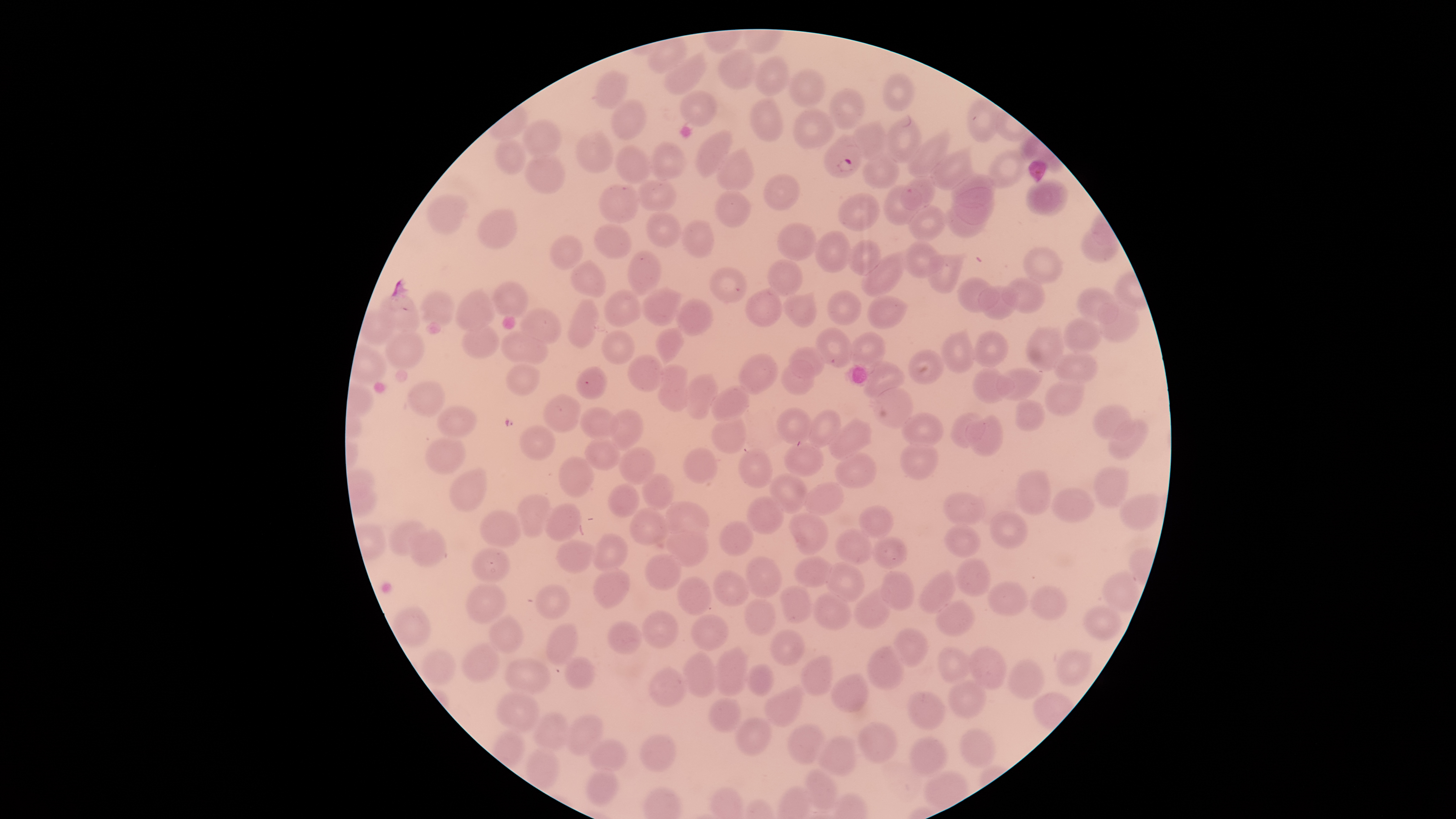
Approximate bounding boxes as [left, top, right, bottom] in pixels. Uninfected red blood cells: [649, 38, 686, 72], [719, 50, 757, 90], [666, 52, 708, 94], [754, 56, 791, 96], [595, 70, 629, 109], [788, 70, 825, 108], [883, 73, 914, 110], [830, 88, 864, 128], [679, 90, 717, 126], [967, 97, 999, 142], [750, 98, 785, 142], [611, 99, 646, 140], [793, 108, 833, 150], [885, 117, 923, 162], [524, 120, 563, 156], [852, 122, 887, 159], [577, 130, 613, 171], [696, 130, 733, 177], [908, 136, 947, 176], [494, 138, 526, 176], [651, 142, 686, 179], [617, 145, 650, 181], [987, 150, 1025, 187], [718, 151, 755, 189], [931, 152, 971, 189], [863, 153, 900, 189], [525, 155, 565, 194], [764, 173, 802, 210], [952, 175, 994, 208], [901, 178, 935, 209], [638, 179, 676, 211], [1026, 180, 1068, 214], [598, 184, 639, 224], [884, 186, 921, 226], [955, 188, 994, 225], [714, 189, 751, 227], [839, 193, 880, 231], [428, 194, 470, 237], [946, 205, 985, 237], [910, 206, 947, 240], [479, 209, 518, 247], [646, 212, 682, 247], [682, 220, 715, 257], [778, 223, 817, 260], [595, 224, 632, 258], [1081, 225, 1119, 263], [816, 231, 851, 271], [550, 235, 585, 269], [847, 241, 881, 276], [903, 241, 943, 279], [1023, 246, 1061, 284], [628, 251, 662, 293], [862, 253, 904, 295], [928, 254, 965, 293], [768, 259, 804, 296], [571, 260, 606, 296], [711, 268, 748, 303], [959, 278, 999, 313], [1003, 278, 1046, 313], [492, 282, 527, 317], [978, 286, 1020, 319], [1077, 286, 1119, 325], [642, 287, 682, 326], [455, 289, 495, 331], [746, 289, 784, 327], [420, 290, 456, 327], [604, 290, 642, 328], [828, 290, 862, 325], [783, 294, 816, 328], [865, 294, 907, 329], [377, 295, 420, 335], [676, 299, 712, 335], [566, 301, 600, 347], [1096, 302, 1139, 341], [520, 307, 561, 345], [359, 308, 396, 346], [1063, 317, 1100, 353], [462, 322, 500, 358], [657, 327, 683, 359], [1026, 327, 1065, 372], [816, 328, 853, 367], [501, 329, 548, 365], [385, 330, 424, 370], [602, 330, 634, 366], [972, 330, 1009, 366], [849, 331, 886, 365], [941, 332, 975, 372], [789, 347, 824, 378], [909, 349, 944, 384], [1053, 352, 1096, 383], [739, 353, 779, 394], [628, 355, 665, 391], [783, 360, 816, 396], [863, 363, 904, 398], [507, 365, 540, 396], [657, 365, 690, 411], [972, 366, 1014, 403], [576, 367, 607, 400], [997, 367, 1044, 399], [683, 374, 719, 417], [1045, 378, 1086, 415], [408, 381, 445, 417], [710, 386, 750, 420], [872, 387, 914, 429], [543, 394, 581, 432], [1013, 400, 1045, 430], [437, 405, 476, 439], [1091, 405, 1132, 440], [580, 406, 618, 438], [778, 408, 812, 443], [807, 408, 841, 445], [609, 409, 643, 447], [901, 412, 943, 447], [951, 413, 985, 448], [712, 414, 747, 455], [965, 415, 1005, 455], [1109, 419, 1148, 458], [829, 420, 873, 459], [520, 425, 556, 460], [427, 435, 466, 475], [584, 437, 620, 471], [786, 437, 823, 475], [900, 442, 940, 478], [618, 447, 655, 483], [686, 448, 717, 484], [740, 448, 773, 488], [836, 451, 877, 487], [558, 456, 592, 497], [1093, 468, 1129, 508], [449, 470, 487, 512], [1017, 470, 1052, 515], [643, 474, 674, 507], [770, 474, 808, 512], [607, 483, 640, 515], [805, 483, 843, 515], [1052, 487, 1095, 523], [944, 491, 987, 526], [515, 494, 551, 538], [1119, 495, 1161, 531], [747, 496, 785, 535], [661, 502, 708, 537], [545, 504, 582, 541], [859, 505, 893, 537], [630, 507, 668, 547], [481, 510, 522, 549], [990, 511, 1028, 549], [790, 513, 827, 555], [390, 520, 425, 555], [719, 520, 753, 556], [944, 526, 980, 558], [410, 529, 447, 567], [836, 529, 874, 565], [665, 530, 709, 566], [591, 533, 628, 569], [872, 536, 907, 570], [557, 539, 595, 573], [473, 547, 510, 583], [646, 554, 683, 590], [745, 556, 782, 599], [793, 557, 833, 587], [956, 557, 992, 597], [827, 563, 863, 602], [594, 566, 631, 609], [714, 570, 749, 607], [919, 570, 957, 613], [881, 571, 914, 611], [1101, 572, 1138, 610], [677, 576, 712, 616], [987, 581, 1029, 616], [466, 584, 505, 625], [535, 585, 569, 620], [779, 585, 812, 624], [1030, 585, 1067, 621], [854, 589, 892, 630], [812, 592, 853, 631], [743, 598, 775, 636], [936, 600, 973, 636], [1083, 605, 1122, 640], [393, 607, 432, 647], [642, 610, 680, 649], [490, 615, 522, 652], [690, 615, 729, 651], [605, 621, 643, 654], [546, 623, 579, 664], [892, 628, 929, 666], [770, 630, 806, 666], [462, 642, 500, 682], [866, 646, 905, 690], [969, 646, 1006, 688], [713, 647, 748, 696], [938, 647, 976, 681], [423, 649, 455, 683], [1056, 650, 1089, 686], [684, 653, 717, 697], [564, 656, 595, 689], [800, 656, 834, 696], [505, 658, 552, 696], [1008, 658, 1044, 698], [745, 663, 774, 696], [647, 667, 689, 708], [832, 674, 869, 712], [948, 681, 986, 719], [764, 688, 803, 727], [497, 691, 540, 733], [906, 691, 946, 732], [708, 697, 740, 733], [533, 713, 572, 751], [567, 714, 603, 755], [735, 718, 771, 756], [858, 721, 899, 763], [786, 724, 829, 765], [958, 729, 995, 769], [639, 733, 675, 773], [818, 737, 856, 776], [910, 737, 949, 777], [590, 739, 627, 774], [528, 750, 560, 791], [585, 769, 619, 807], [804, 770, 837, 810]. Parasitized red blood cells: [824, 134, 862, 177]. Thin blood film. Image is 1456×819 pixels. Giemsa stain. Photographed with a smartphone camera through the microscope eyepiece. Circular visible region. Presence: malaria parasites detected. Species: Plasmodium falciparum. One field of view of the specimen.